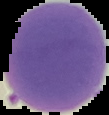

image size = 109×115 pixels
image type = segmented cell region with the area outside set to black
result = negative for Plasmodium parasites
preparation = thin blood smear